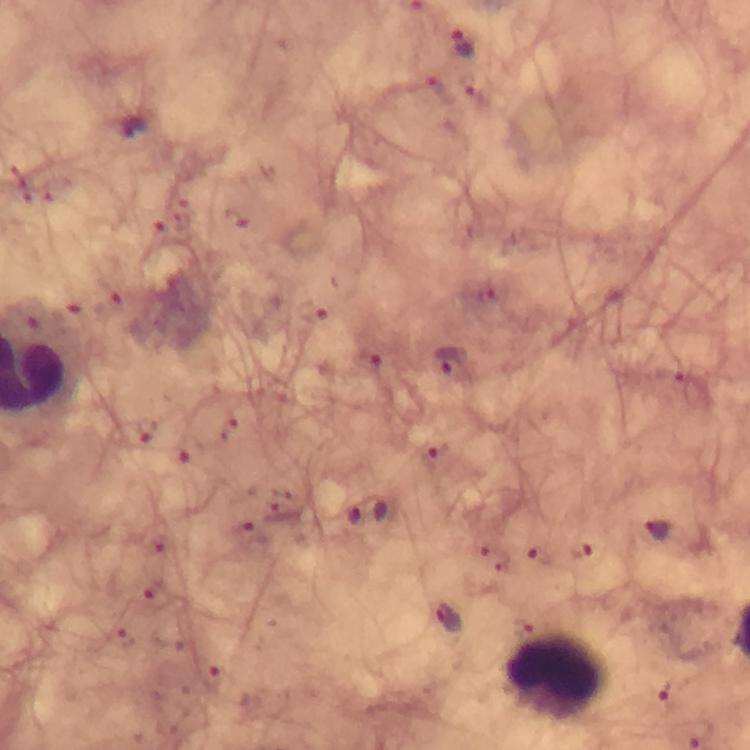
context = from a diagnostic examination for malaria
cropped from = a single field of view
image size = 750×750 pixels
capture = smartphone mounted on the microscope
stain = Giemsa
leukocyte locations = approximate centers as (x, y) in pixels: (558, 676)
magnification = 100x
Plasmodium parasite locations = approximate centers as (x, y) in pixels: (462, 44), (448, 362), (147, 433), (433, 455), (367, 511), (654, 528), (448, 620), (671, 690)
preparation = thick blood film
immersion oil = used